Mark where platelets are.
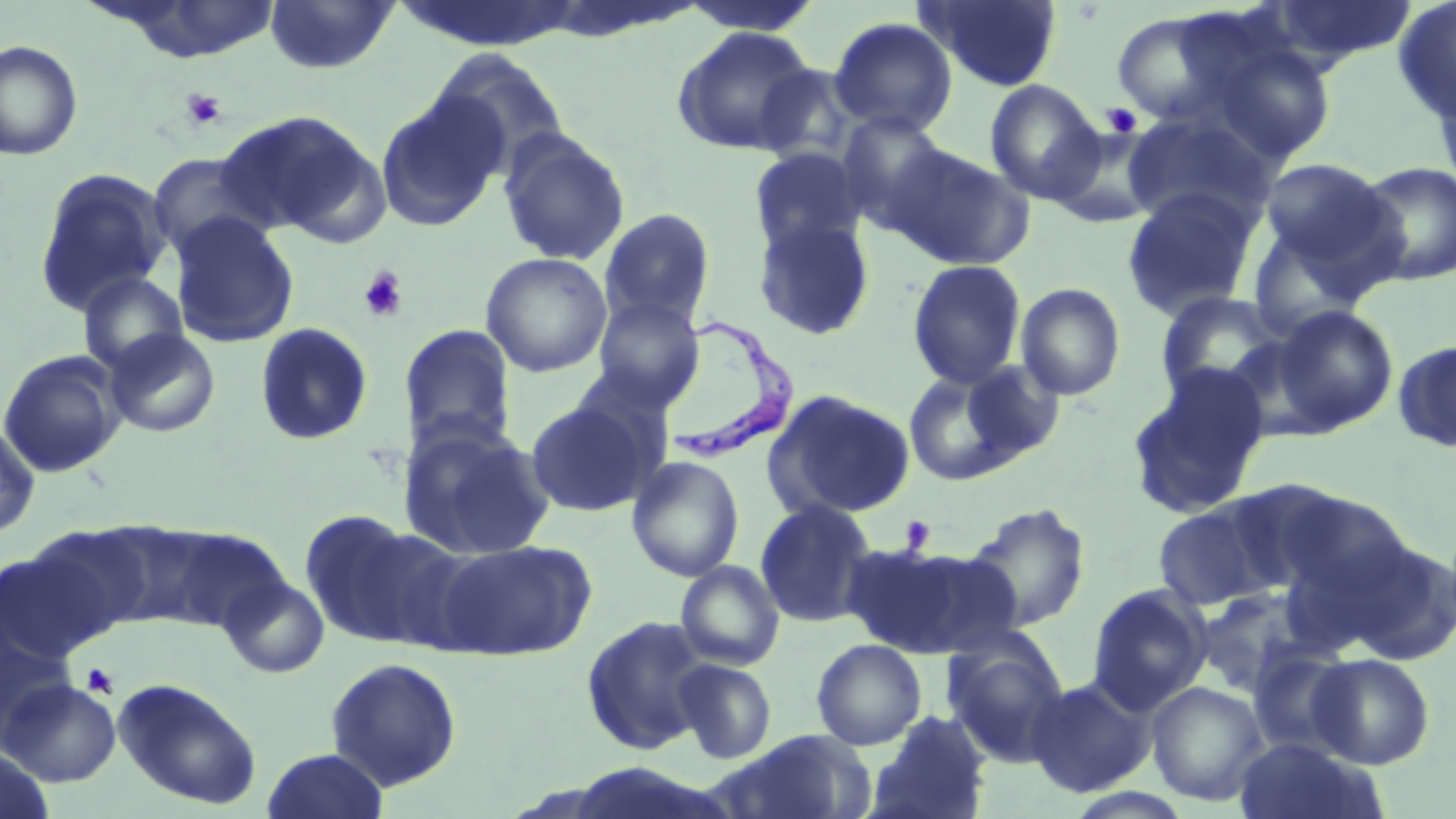
Approximate bounding boxes as (x1,y1)-(x2,y2) corner pairs in pixels.
Platelets: (180,89)-(226,130), (1101,102)-(1141,137), (358,267)-(409,323), (899,515)-(936,552), (82,662)-(119,698).

slide-level diagnosis = Trypanosoma brucei
field of view = single
preparation = thin blood smear
Trypanosoma brucei locations = approximate bounding boxes as (x1,y1)-(x2,y2) corner pairs in pixels: (666,312)-(804,460)
uninfected red blood cell locations = approximate bounding boxes as (x1,y1)-(x2,y2) corner pairs in pixels: (103,0)-(284,63), (264,0)-(399,75), (918,0)-(1064,92), (1262,0)-(1417,70), (1393,1)-(1456,124), (674,2)-(825,36), (1110,7)-(1266,131), (829,17)-(957,137), (671,25)-(820,157), (0,40)-(83,161), (1207,40)-(1337,164), (429,48)-(571,178), (1431,71)-(1456,200), (985,79)-(1105,204), (376,91)-(508,232), (215,110)-(378,239), (1122,112)-(1274,229), (836,113)-(957,233), (1049,126)-(1166,227), (498,131)-(631,266), (887,144)-(1036,271), (748,147)-(867,256), (147,154)-(273,261), (1257,158)-(1398,280), (1353,160)-(1456,286), (33,167)-(173,316), (1121,187)-(1261,322), (599,208)-(716,330), (169,214)-(300,347), (753,216)-(876,341), (1244,220)-(1374,338), (480,251)-(613,378), (907,259)-(1027,389), (77,271)-(189,376), (1015,282)-(1126,401), (1155,291)-(1291,401), (591,297)-(705,411), (1271,304)-(1398,435), (254,322)-(374,447), (399,324)-(517,451), (104,328)-(221,438), (1393,339)-(1456,454), (0,351)-(127,477), (957,360)-(1066,465), (1126,365)-(1270,518), (902,367)-(1027,486), (765,388)-(917,521), (525,398)-(656,517), (399,421)-(555,560), (0,423)-(40,540), (626,455)-(745,582), (1221,479)-(1353,591), (1271,488)-(1414,609), (1152,497)-(1284,611), (755,499)-(878,628), (963,502)-(1091,632), (301,514)-(455,650), (87,520)-(209,627), (24,524)-(152,642), (1338,536)-(1456,667), (434,539)-(596,661), (851,543)-(1023,659), (675,560)-(786,671), (219,574)-(330,679), (1086,584)-(1212,714), (1194,586)-(1323,698), (581,614)-(712,755), (942,636)-(1071,766), (811,638)-(927,750), (1247,647)-(1358,758), (1308,653)-(1435,770), (325,656)-(462,792), (673,658)-(777,764), (1025,675)-(1158,798), (113,676)-(263,810), (1,678)-(121,786), (1147,681)-(1270,806), (866,710)-(993,819), (722,729)-(877,819), (1233,737)-(1382,819), (0,747)-(54,818), (262,747)-(388,819)
magnification = 1000x
image size = 1456×819 pixels
stain = May-Grünwald-Giemsa
modality = optical microscopy